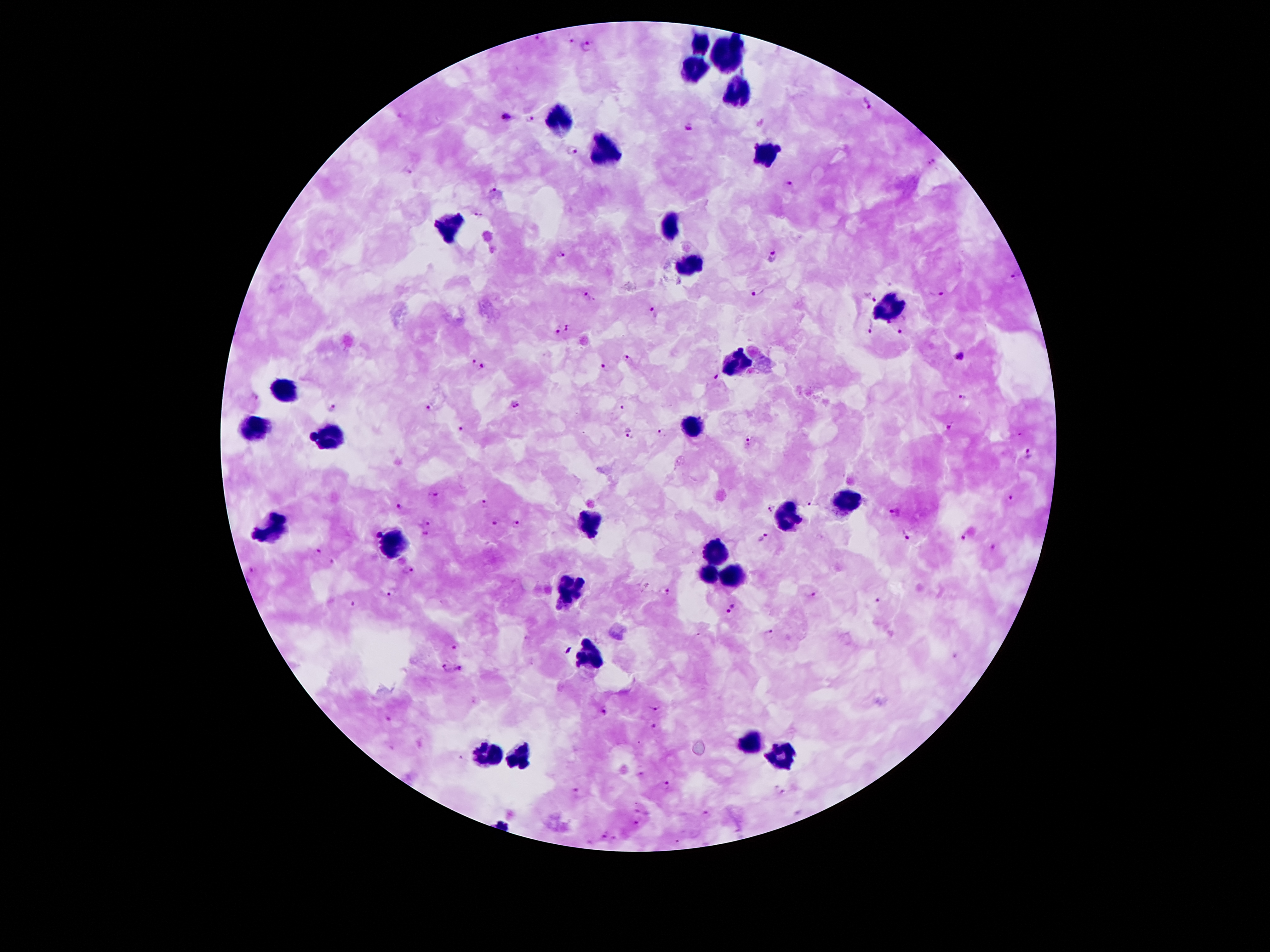
Approximate centers as (x, y) in pixels. Leukocyte locations: (701, 45), (730, 58), (694, 67), (737, 92), (560, 118), (606, 152), (765, 152), (449, 226), (671, 226), (692, 265), (891, 308), (739, 360), (285, 392), (694, 426), (258, 429), (333, 435), (846, 500), (787, 515), (588, 519), (271, 528), (399, 547), (716, 553), (707, 574), (731, 574), (567, 587), (592, 660), (751, 742), (487, 753), (518, 757), (783, 757). Malaria parasite locations: (538, 37), (574, 40), (588, 44), (867, 102), (506, 115), (530, 116), (688, 128), (755, 143), (780, 147), (572, 151), (931, 164), (408, 171), (789, 184), (494, 189), (478, 214), (559, 252), (771, 256), (1015, 275), (757, 292), (936, 294), (589, 295), (871, 298), (653, 311), (872, 326), (567, 327), (897, 328), (555, 330), (960, 354), (628, 358), (469, 361), (604, 366), (482, 367), (717, 376), (254, 397), (963, 397), (428, 404), (515, 404), (621, 404), (333, 407), (950, 427), (461, 429), (663, 432), (630, 434), (310, 435), (748, 443), (1028, 454), (434, 495), (1011, 497), (808, 502), (485, 503), (399, 506), (770, 507), (896, 511), (431, 521), (497, 522), (513, 524), (964, 533), (378, 534), (424, 534), (906, 534), (762, 536), (996, 547), (317, 550), (333, 563), (254, 570), (409, 571), (392, 592), (668, 592), (814, 595), (878, 601), (353, 604), (731, 608), (770, 631), (454, 648), (569, 650), (459, 668), (447, 669), (655, 707), (605, 710), (386, 716), (654, 726), (664, 784), (776, 787), (577, 792), (784, 793), (638, 810), (706, 814), (637, 821), (604, 834), (614, 838). Single field of view. Smartphone photograph taken through the microscope eyepiece. Patient malaria status: positive for Plasmodium falciparum. Giemsa-stained preparation. Thick blood film. 100x magnification. Image is 1270×952 pixels.